Classify this cell by malaria status.
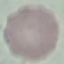

It is uninfected.

Cell patch, automatically extracted from a larger field of view and resized to 64 × 64 pixels. Photographed with a smartphone camera at the microscope eyepiece. Giemsa stain. Thin blood smear.